Point out each leukocyte.
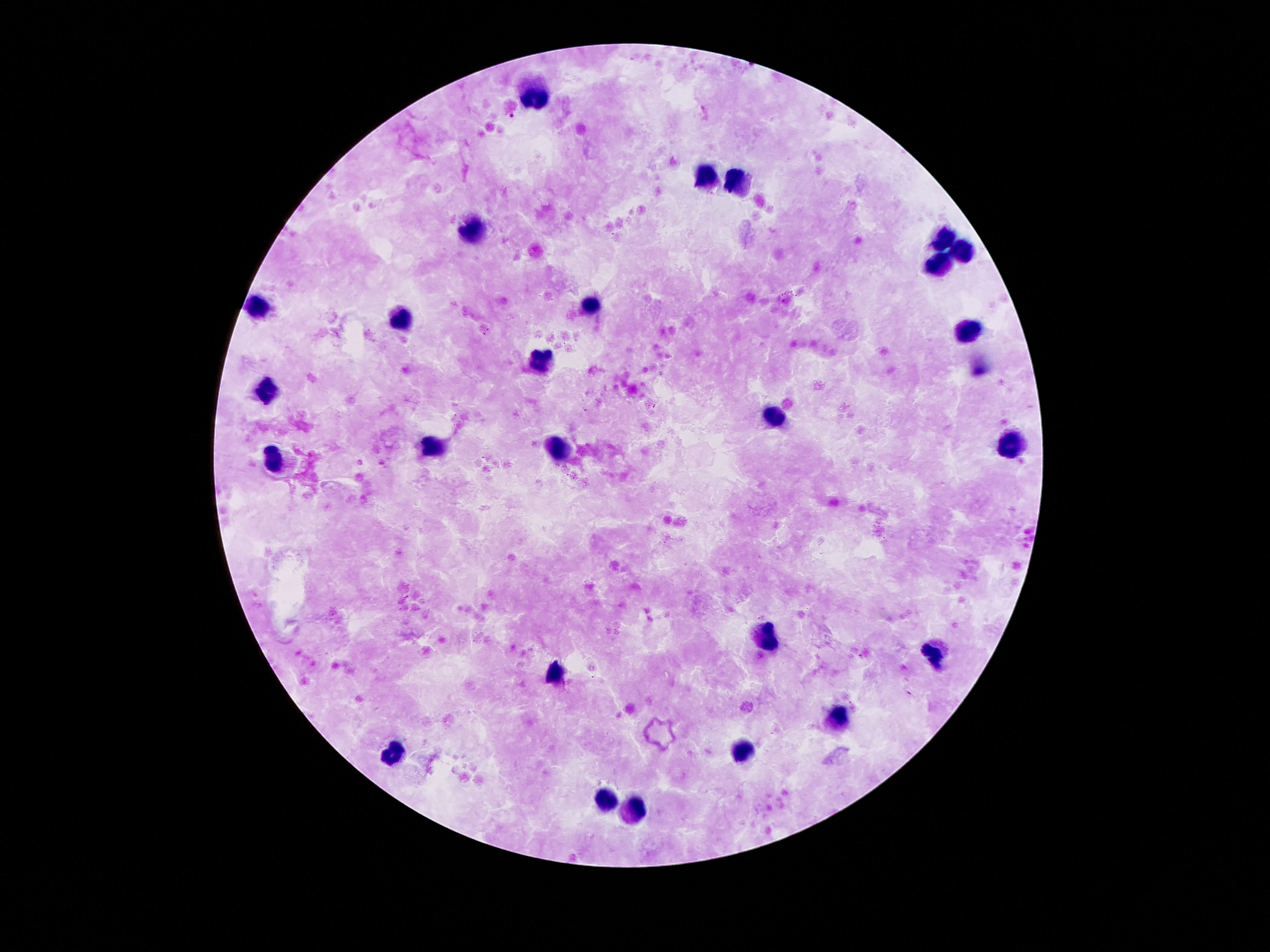

Approximate object centers, in pixels from the top-left corner.
Leukocytes: (x=540, y=96), (x=708, y=173), (x=740, y=180), (x=472, y=225), (x=950, y=235), (x=966, y=248), (x=940, y=261), (x=591, y=302), (x=255, y=306), (x=394, y=319), (x=969, y=332), (x=543, y=357), (x=265, y=390), (x=775, y=419), (x=1011, y=445), (x=433, y=448), (x=562, y=451), (x=275, y=461), (x=769, y=632), (x=930, y=654), (x=556, y=671), (x=840, y=726), (x=740, y=748), (x=391, y=751), (x=601, y=797), (x=636, y=809).

capture = smartphone camera through the microscope eyepiece
stain = Giemsa
magnification = 100x
field of view = single
preparation = thick blood smear
patient malaria status = negative
image size = 1270×952 pixels